Give the preparation type.
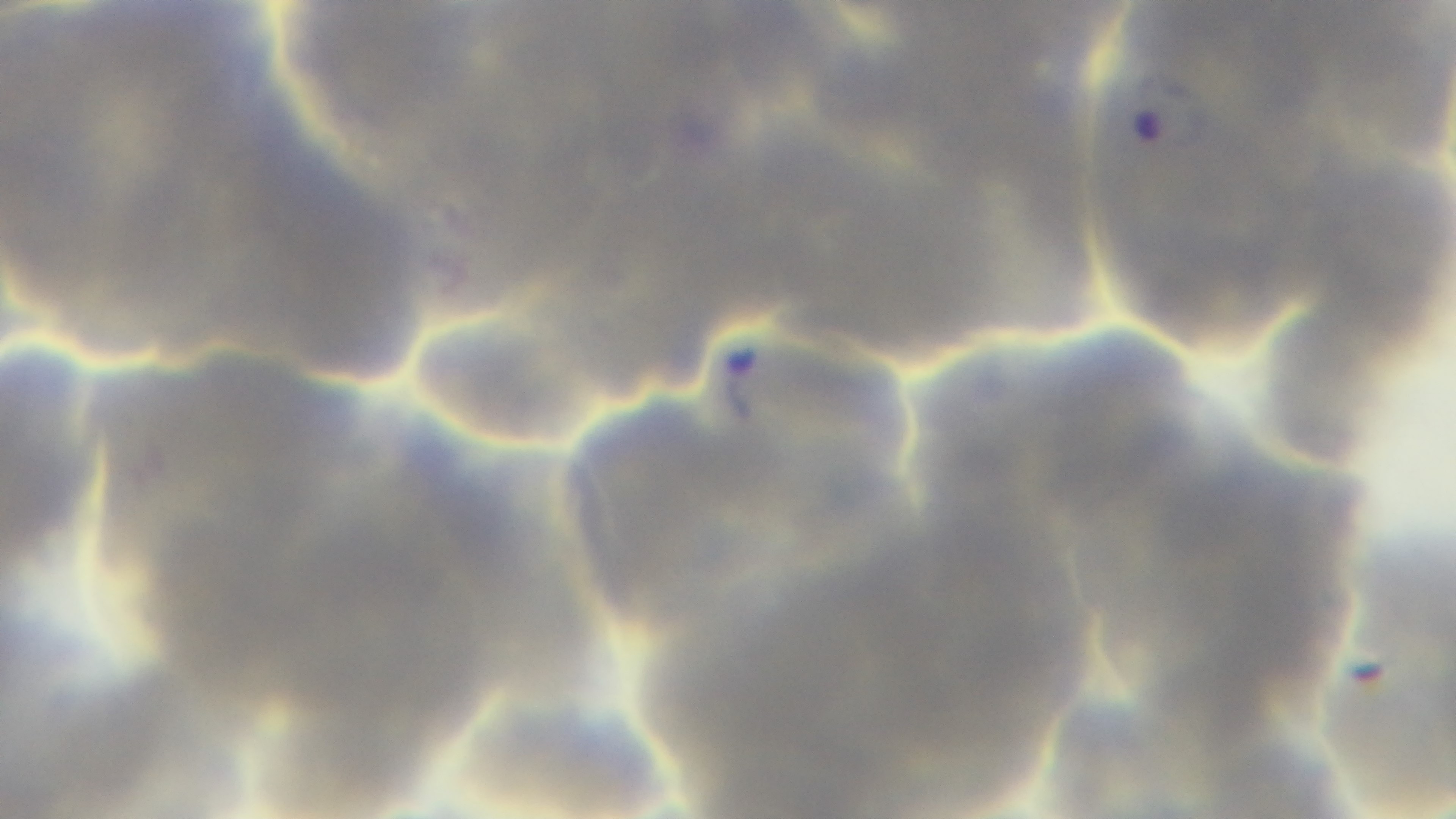

Thin.

Summary:
  - Modality: light microscopy
  - Capture: mounted 4K digital camera
  - Malaria status: positive
  - Stain: Giemsa
  - Field of view: single
  - Objective: 100x oil immersion